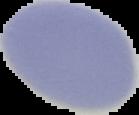

image size = 139×115 pixels
preparation = thin blood film
image type = segmented cell region on a black background
result = no Plasmodium parasites seen